Name the parasite shown.
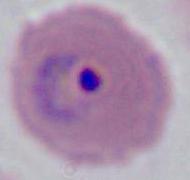

This is Plasmodium.

Summary:
  - Magnification: 400x or 1000x
  - Modality: photomicrograph